State which cell type is depicted.
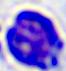
This is a leukocyte.

Photomicrograph. Captured at 400x magnification.